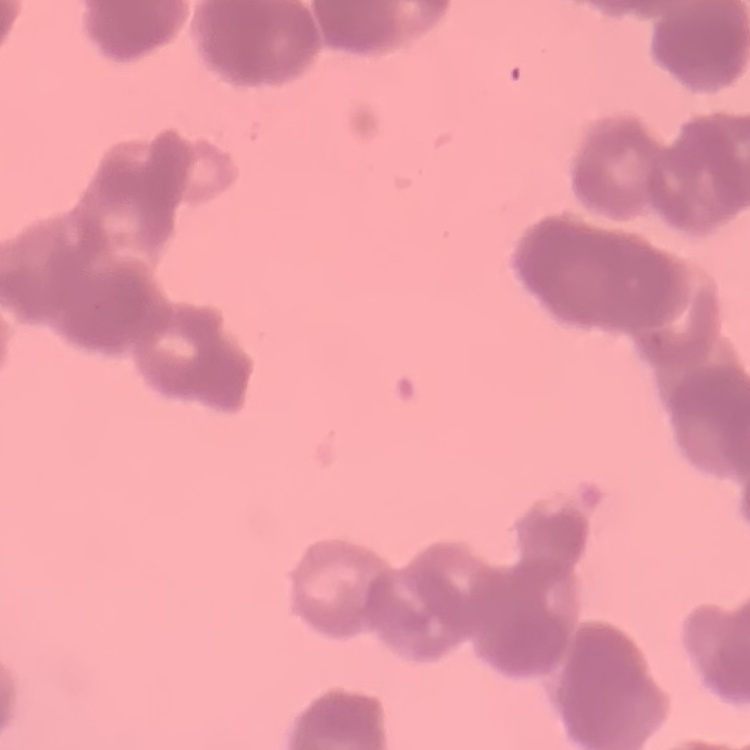 The red blood cells exhibit rouleaux formation. One tile cut from a larger photomicrograph. Field's or Giemsa stain. Thin blood film.